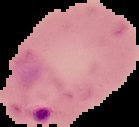 Result: Plasmodium parasites identified. From a thin blood smear. Image is 139×127 pixels. The area outside the segmented cell region is set to black.